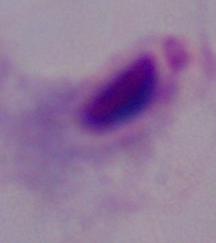
modality = photomicrograph
magnification = 1000x
identification = trichomonad